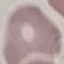
Summary:
  - Malaria status: uninfected
  - Capture: smartphone camera at the microscope eyepiece
  - Stain: Giemsa
  - Image type: automatically extracted cell patch, resized to 64 × 64 pixels
  - Preparation: thin blood smear